Identify the blood parasite species.
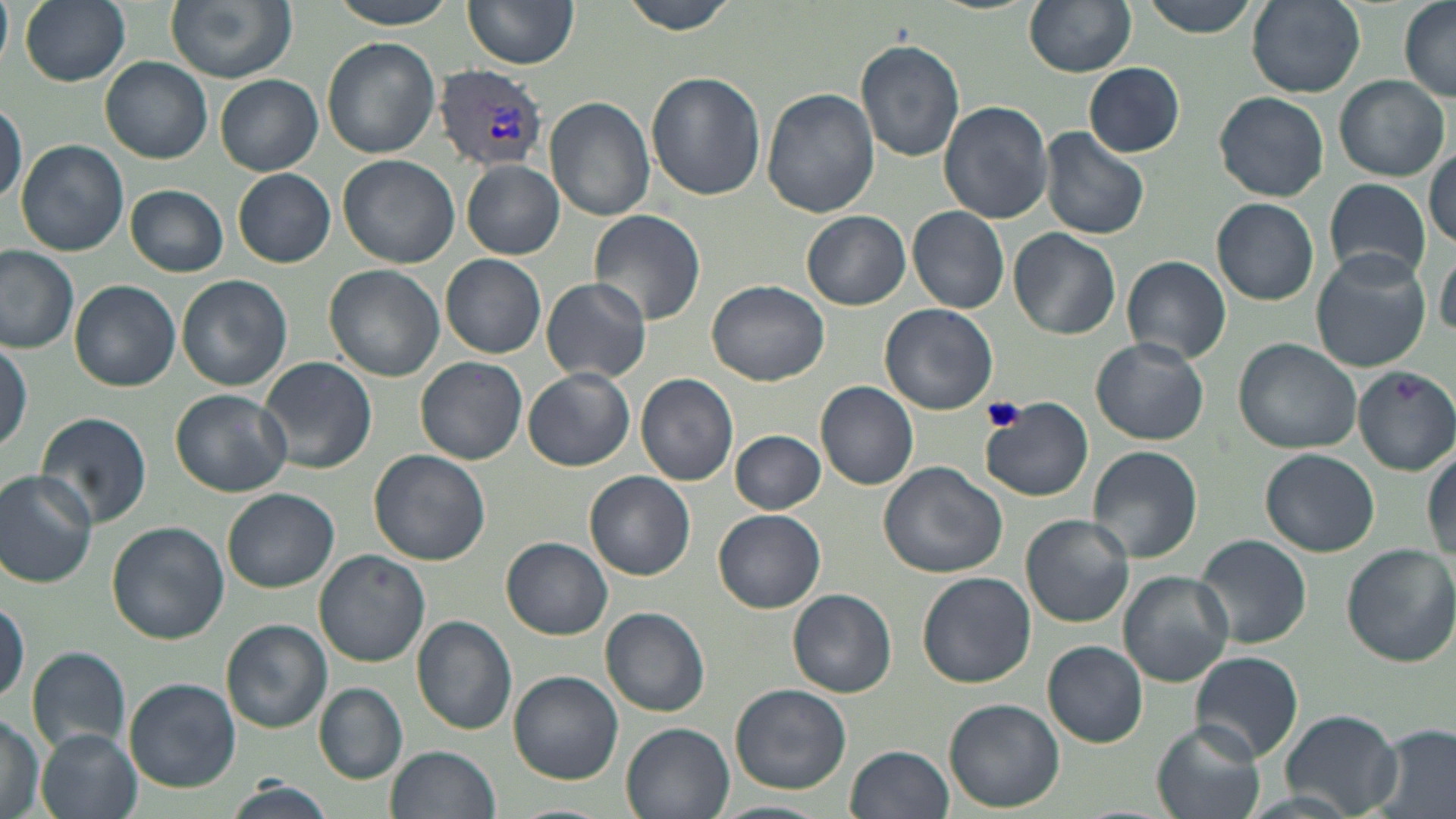
Plasmodium vivax.

Summary:
  - Coordinate format: approximate bounding boxes as [x1, y1, x2, y2] in pixels
  - Uninfected red blood cell locations: [0, 0, 12, 69], [20, 0, 130, 86], [163, 0, 296, 82], [330, 0, 456, 28], [462, 0, 581, 69], [619, 0, 741, 35], [1024, 0, 1138, 76], [1135, 0, 1261, 36], [1247, 0, 1366, 96], [1399, 1, 1456, 101], [321, 37, 440, 158], [856, 38, 966, 163], [101, 56, 212, 163], [1084, 61, 1186, 157], [215, 72, 323, 176], [645, 72, 766, 201], [1333, 75, 1449, 181], [762, 87, 879, 218], [1214, 91, 1328, 202], [546, 96, 654, 221], [938, 99, 1054, 224], [0, 100, 26, 209], [1038, 126, 1150, 241], [16, 139, 129, 257], [1426, 149, 1455, 249], [339, 155, 460, 269], [461, 161, 565, 259], [233, 169, 335, 268], [1323, 179, 1430, 284], [127, 185, 228, 276], [1211, 198, 1319, 304], [908, 206, 1009, 313], [589, 209, 707, 327], [802, 211, 911, 310], [1010, 229, 1120, 341], [1435, 242, 1455, 339], [0, 246, 80, 352], [1310, 249, 1431, 372], [441, 254, 546, 358], [1122, 257, 1231, 362], [324, 265, 446, 383], [176, 274, 292, 391], [539, 277, 652, 383], [707, 279, 830, 386], [71, 281, 180, 392], [881, 304, 998, 416], [0, 338, 31, 452], [1091, 338, 1210, 444], [1233, 339, 1362, 454], [260, 355, 377, 475], [416, 357, 528, 464], [1353, 364, 1456, 474], [524, 368, 635, 472], [635, 373, 738, 487], [816, 381, 918, 490], [169, 389, 292, 497], [983, 400, 1093, 502], [37, 410, 152, 530], [730, 430, 827, 514], [1086, 446, 1201, 565], [1262, 448, 1381, 558], [1423, 448, 1456, 567], [368, 449, 490, 566], [877, 461, 1008, 578], [0, 470, 101, 589], [585, 471, 695, 581], [223, 488, 342, 594], [713, 509, 826, 613], [1021, 514, 1134, 626], [107, 522, 230, 644], [1196, 535, 1312, 649], [500, 537, 613, 640], [1341, 542, 1456, 666], [313, 549, 430, 666], [917, 571, 1036, 687], [1119, 571, 1233, 686], [788, 588, 897, 696], [0, 599, 27, 707], [599, 607, 710, 717], [411, 616, 516, 734], [222, 620, 331, 732], [1042, 640, 1148, 747], [27, 646, 131, 756], [1189, 651, 1303, 762], [511, 671, 623, 785], [124, 679, 239, 793], [315, 683, 407, 783], [730, 684, 852, 796], [944, 699, 1065, 812], [0, 709, 45, 819], [1282, 709, 1402, 817], [1152, 721, 1263, 819], [621, 722, 736, 819], [1368, 724, 1456, 819], [37, 729, 142, 819], [845, 744, 954, 819], [386, 745, 500, 819], [225, 780, 333, 819], [713, 800, 833, 819], [507, 804, 612, 819]
  - Plasmodium vivax-infected red blood cell locations: [434, 65, 548, 170]
  - Platelet locations: [981, 396, 1026, 433]
  - Stain: May-Grünwald-Giemsa
  - Preparation: thin blood smear
  - Modality: light microscopy
  - Image size: 1456×819 pixels
  - Magnification: 1000x
  - Field of view: one of a larger specimen